Locate every blood parasite and identify its species.
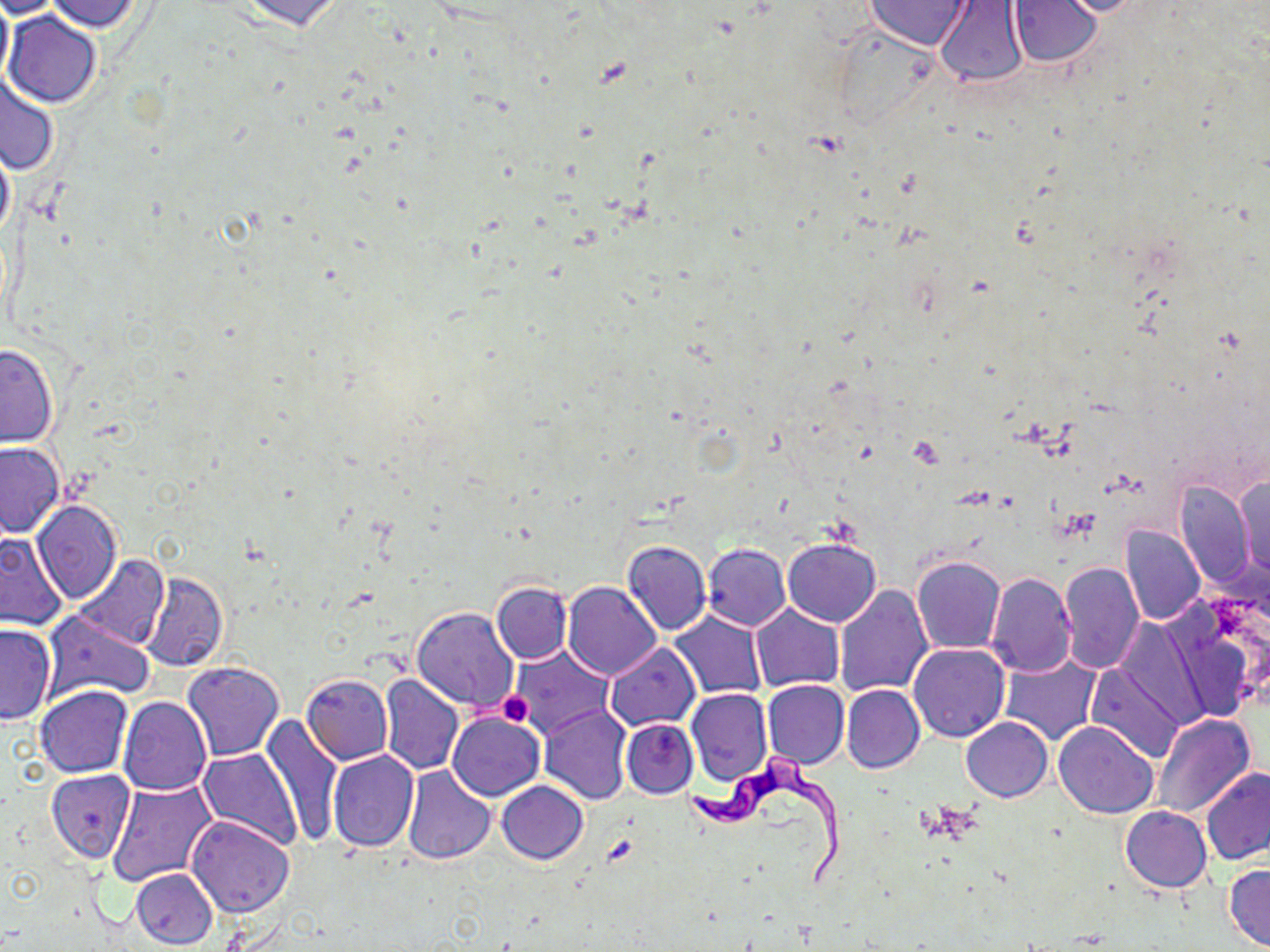

Approximate bounding boxes as (x1, y1, x2, y2) in pixels.
Trypanosoma brucei: (683, 752, 842, 888).
No Plasmodium falciparum, Plasmodium ovale, Plasmodium malariae, Plasmodium vivax, or Babesia divergens observed.

Platelet locations: (907, 434, 945, 467), (498, 692, 533, 727). Uninfected red blood cell locations: (0, 0, 13, 94), (0, 0, 64, 20), (230, 0, 349, 33), (1041, 0, 1156, 18), (45, 1, 147, 34), (863, 1, 974, 51), (1008, 1, 1104, 68), (933, 2, 1032, 89), (5, 11, 102, 108), (2, 73, 60, 175), (0, 137, 15, 243), (0, 342, 60, 447), (0, 442, 65, 537), (1233, 475, 1269, 580), (1172, 480, 1254, 590), (32, 499, 122, 603), (1119, 524, 1206, 627), (0, 533, 69, 631), (783, 537, 880, 627), (622, 540, 712, 635), (702, 543, 791, 630), (72, 555, 169, 651), (912, 556, 1006, 654), (1058, 559, 1143, 675), (140, 572, 227, 673), (984, 572, 1076, 677), (491, 582, 571, 664), (562, 582, 662, 679), (834, 586, 933, 696), (1162, 598, 1262, 725), (750, 604, 843, 690), (411, 606, 520, 715), (42, 610, 154, 705), (667, 612, 769, 700), (1115, 619, 1212, 728), (0, 624, 56, 725), (605, 641, 700, 731), (908, 642, 1009, 742), (510, 646, 614, 740), (999, 654, 1102, 747), (181, 661, 284, 760), (1086, 662, 1186, 763), (301, 674, 392, 764), (380, 674, 463, 775), (761, 679, 848, 770), (35, 684, 132, 778), (841, 684, 924, 773), (687, 688, 773, 786), (118, 697, 210, 796), (538, 706, 632, 804), (448, 712, 545, 801), (1149, 714, 1257, 819), (260, 715, 343, 848), (960, 717, 1051, 802), (622, 718, 698, 798), (1053, 721, 1158, 819), (197, 748, 300, 849), (328, 750, 420, 852), (402, 767, 496, 864), (1201, 768, 1270, 865), (45, 769, 134, 862), (108, 779, 220, 889), (497, 780, 588, 864), (1119, 806, 1212, 892), (186, 815, 296, 918), (1224, 864, 1270, 950), (131, 868, 217, 949). Slide-level diagnosis: Trypanosoma brucei. May-Grünwald-Giemsa stain. Optical microscopy. Image is 1270×952 pixels. Captured at 1000x magnification. Thin blood film. Single field of view.